Draw a bounding box around every leukocyte (white blood cell).
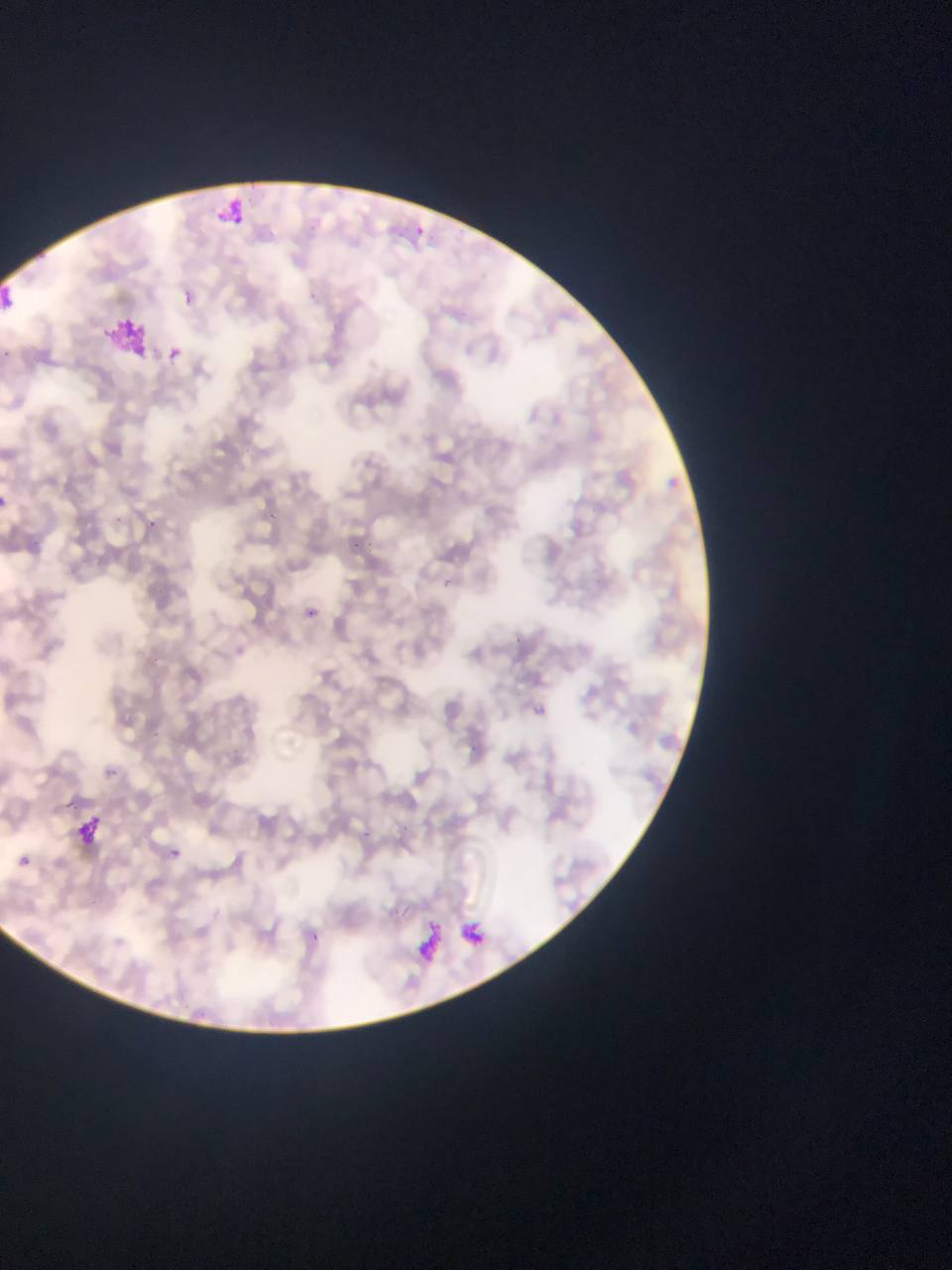
No leukocytes observed.

malaria_parasite_locations: 'approximate bounding boxes as (left, top, right, bottom) in pixels: (166, 348, 182, 362), (266, 506, 285, 524), (147, 515, 160, 533), (113, 516, 134, 528), (355, 538, 372, 558), (443, 575, 456, 594), (307, 603, 323, 621), (534, 703, 548, 716), (105, 767, 117, 777), (400, 823, 414, 834), (357, 828, 375, 845), (166, 846, 193, 861), (19, 856, 31, 868), (310, 930, 316, 943)'
artifact_stain_precipitate_or_debris_locations: 'approximate bounding boxes as (left, top, right, bottom) in pixels: (218, 193, 262, 226), (0, 275, 23, 314), (103, 313, 155, 362), (67, 805, 107, 859), (405, 917, 450, 962), (457, 917, 483, 951)'
preparation: thin blood film
image_size: 952×1270 pixels
capture: mobile-phone photograph through a microscope
field_of_view: single
country: Ghana